Comment on the morphology of the erythrocytes.
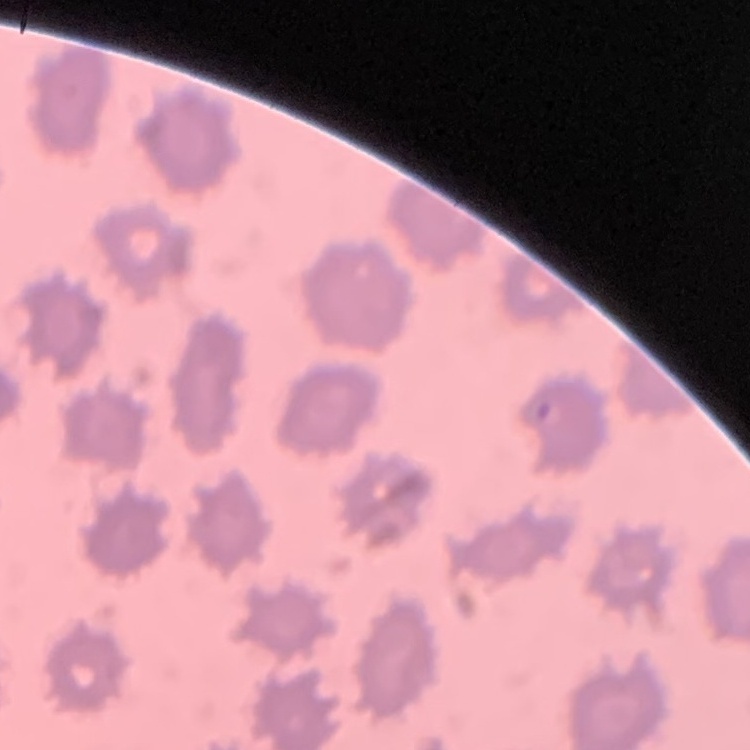
They show no rouleaux formation.

Square crop of a larger photomicrograph. Field's or Giemsa stain. Thin peripheral smear.